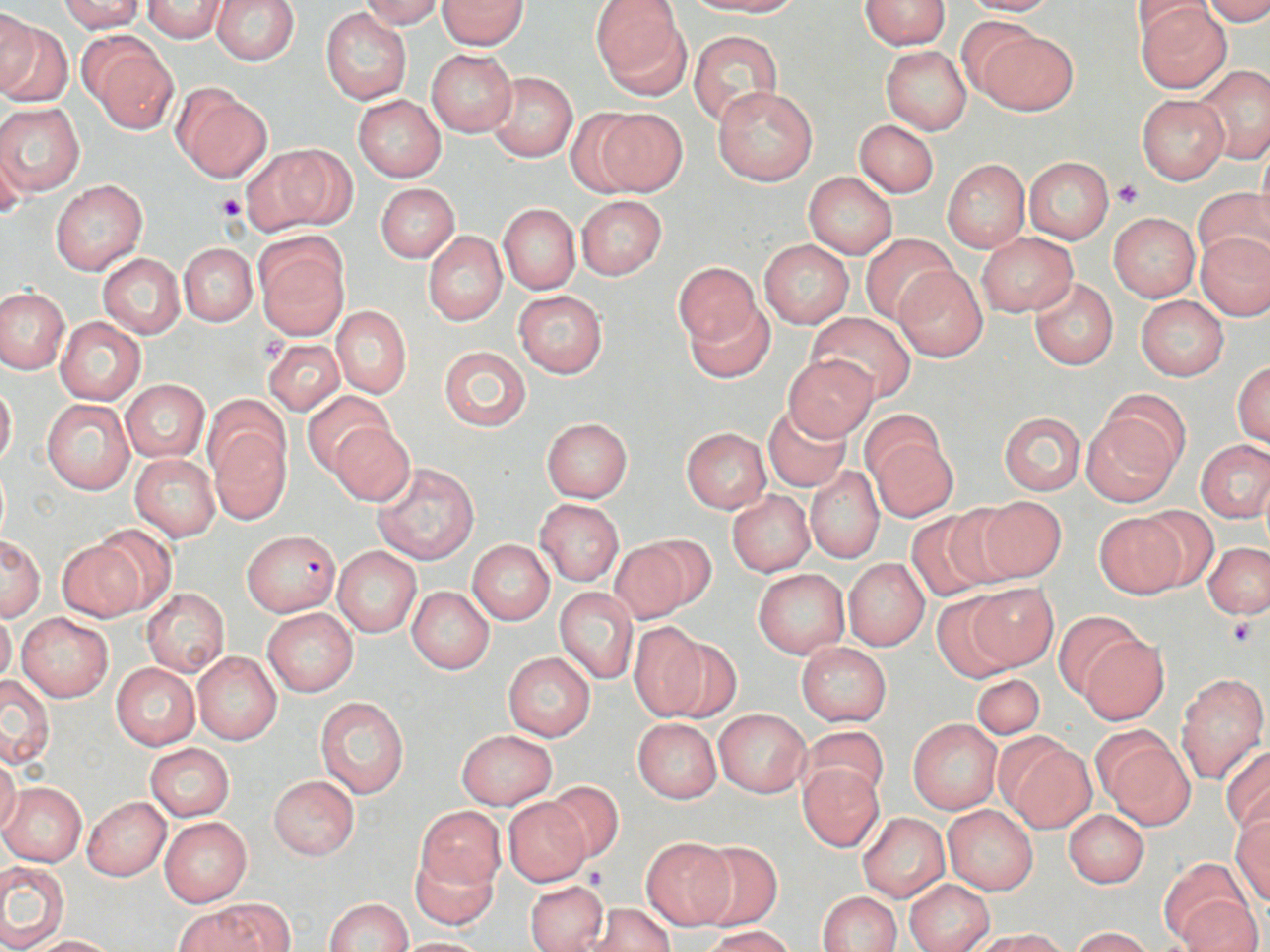

slide-level diagnosis = Plasmodium falciparum
stain = May-Grünwald-Giemsa
image size = 1270×952 pixels
preparation = thin blood film
modality = light microscopy
Plasmodium falciparum-infected red blood cell locations = approximate bounding boxes as (x1,y1)-(x2,y2) corner pairs in pixels: (242,528)-(343,618)
magnification = 1000x
uninfected red blood cell locations = approximate bounding boxes as (x1,y1)-(x2,y2) corner pairs in pixels: (59,0)-(146,32), (211,0)-(299,65), (359,0)-(443,29), (438,0)-(528,49), (593,0)-(688,96), (694,0)-(804,16), (859,0)-(950,50), (957,0)-(1061,16), (1128,0)-(1218,41), (1203,0)-(1270,26), (141,1)-(228,42), (1135,1)-(1234,93), (0,8)-(39,96), (321,8)-(412,105), (1,18)-(71,109), (972,26)-(1079,116), (689,30)-(784,129), (84,37)-(178,132), (880,45)-(970,135), (426,50)-(516,136), (1195,65)-(1270,164), (486,71)-(578,162), (712,85)-(818,186), (172,87)-(273,182), (1137,93)-(1229,183), (353,95)-(446,182), (0,101)-(85,197), (590,107)-(687,197), (854,119)-(939,198), (1,138)-(28,218), (246,145)-(353,234), (1253,145)-(1270,241), (1023,157)-(1114,243), (942,159)-(1030,252), (803,173)-(898,259), (49,179)-(148,276), (375,183)-(459,262), (1192,186)-(1270,270), (576,196)-(667,280), (497,204)-(581,295), (1109,213)-(1200,301), (1196,231)-(1270,321), (424,232)-(507,326), (860,232)-(958,324), (976,233)-(1077,316), (255,237)-(349,337), (759,241)-(853,328), (179,242)-(256,326), (98,253)-(186,339), (673,263)-(762,351), (896,266)-(987,362), (1028,276)-(1119,370), (0,288)-(68,373), (515,291)-(607,377), (1135,295)-(1229,380), (0,297)-(128,387), (685,299)-(774,382), (332,306)-(411,398), (806,311)-(916,403), (55,317)-(146,405), (266,323)-(411,405), (263,338)-(345,414), (438,346)-(532,431), (783,355)-(876,440), (1233,361)-(1270,448), (121,379)-(209,463), (0,381)-(16,470), (302,390)-(392,477), (1103,390)-(1190,475), (203,395)-(290,482), (42,399)-(136,495), (762,405)-(851,491), (860,410)-(945,489), (1082,410)-(1182,506), (999,412)-(1085,495), (542,418)-(632,502), (209,422)-(291,522), (329,422)-(415,506), (680,427)-(771,513), (868,432)-(959,521), (1197,440)-(1270,521), (132,454)-(220,541), (372,462)-(478,564), (804,465)-(885,564), (734,478)-(881,568), (727,491)-(813,577), (971,496)-(1068,582), (536,500)-(623,585), (1134,506)-(1222,591), (906,512)-(1000,602), (1095,514)-(1185,598), (88,527)-(177,614), (615,534)-(712,621), (0,536)-(44,620), (58,540)-(145,621), (468,540)-(554,624), (1203,543)-(1268,618), (333,548)-(421,637), (844,559)-(929,650), (752,569)-(850,658), (968,583)-(1058,671), (406,586)-(494,673), (555,588)-(639,683), (142,589)-(230,675), (931,592)-(1020,682), (0,608)-(17,687), (263,609)-(358,696), (1052,610)-(1144,699), (17,614)-(113,701), (627,622)-(713,720), (1078,633)-(1170,724), (660,636)-(742,722), (796,643)-(891,726), (192,652)-(281,744), (503,652)-(596,741), (111,662)-(200,750), (1176,673)-(1268,782), (1,674)-(55,767), (972,674)-(1045,740), (315,696)-(409,799), (714,709)-(811,797), (632,718)-(721,802), (907,718)-(1002,815), (800,724)-(887,804), (457,729)-(557,810), (1095,731)-(1194,827), (995,735)-(1094,832), (145,743)-(235,821), (1219,746)-(1270,834), (0,752)-(21,837), (798,765)-(884,851), (269,775)-(359,860), (1,782)-(87,866), (544,782)-(624,863), (83,797)-(171,881), (502,799)-(588,885), (941,804)-(1039,895), (416,805)-(505,889), (1063,809)-(1150,887), (857,813)-(950,901), (1229,816)-(1270,904), (159,817)-(252,906), (640,838)-(736,930), (693,843)-(783,932), (409,847)-(498,931), (1158,858)-(1251,946), (0,862)-(68,949), (524,879)-(609,951), (903,880)-(994,951), (816,891)-(901,952), (1177,897)-(1261,952), (323,898)-(413,952), (194,899)-(293,951), (585,903)-(676,950), (704,926)-(795,952), (1072,927)-(1154,952), (979,929)-(1067,952), (25,935)-(119,952), (387,937)-(492,951)
platelet locations = approximate bounding boxes as (x1,y1)-(x2,y2) corner pairs in pixels: (1112,179)-(1145,209), (217,193)-(247,221), (259,336)-(287,364), (1226,616)-(1261,649), (581,865)-(610,889)
field of view = single